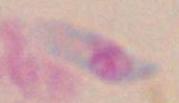
Toxoplasma gondii is shown. Photomicrograph. 1000x magnification.